Assess this cell for malaria.
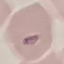

Uninfected.

image_type: cell patch, automatically extracted from a larger field of view and resized to 64 × 64 pixels
stain: Giemsa
preparation: thin smear
capture: smartphone camera at the microscope eyepiece